State which parasite is depicted.
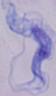

A trypanosome.

Micrograph. 1000x magnification.